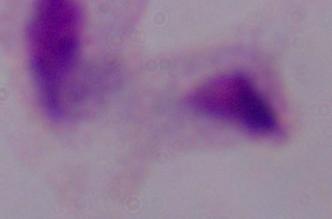

{
  "modality": "micrograph",
  "magnification": "1000x",
  "identification": "trichomonad"
}